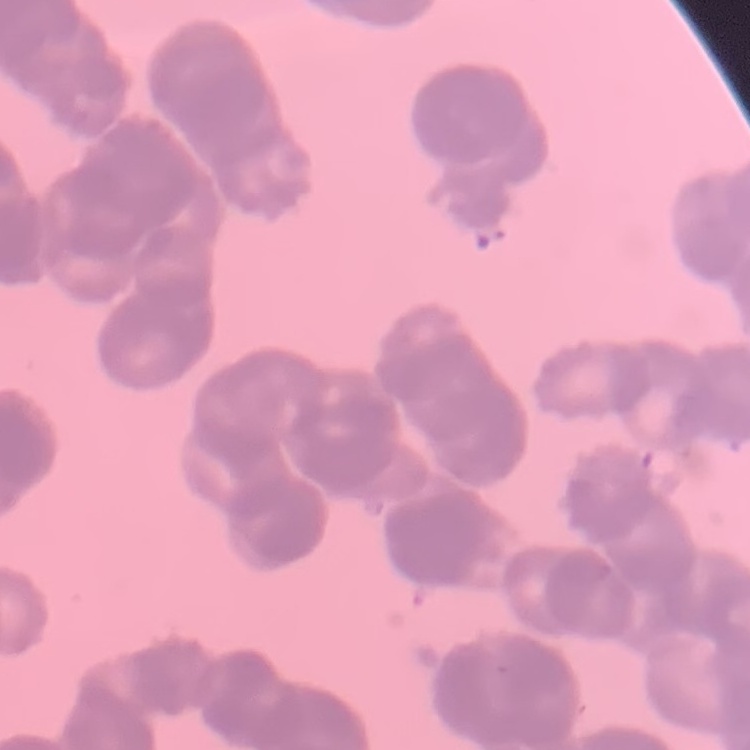

The red blood cells show rouleaux formation. One tile cut from a larger photomicrograph. Field's or Giemsa stain. Thin peripheral smear.